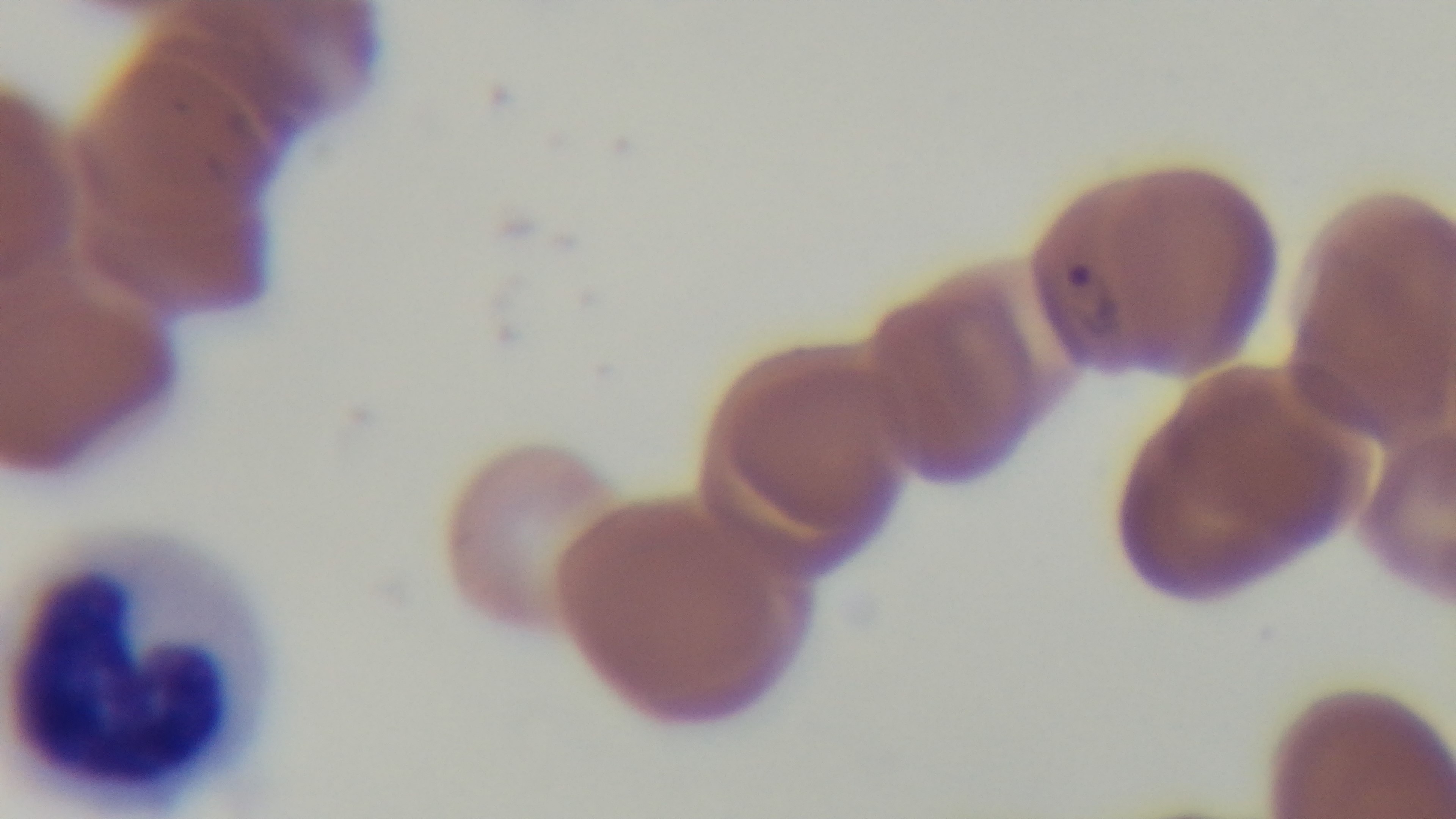

field_of_view: one from the slide
objective: 100x oil immersion
preparation: thin
capture: mounted 4K digital camera
malaria_status: infected
stain: Giemsa
modality: light microscopy